State the blood parasite species.
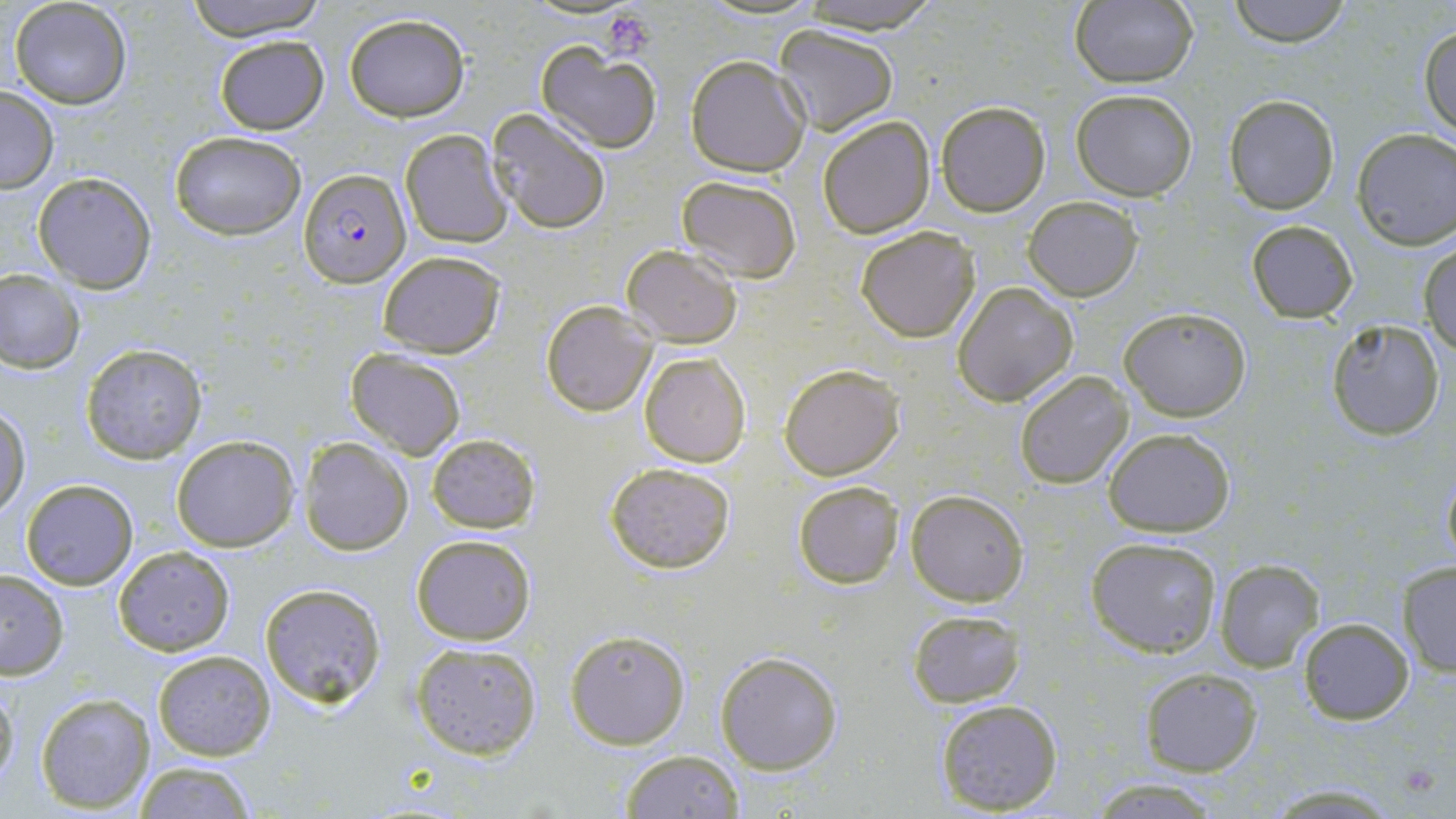

Plasmodium falciparum.

Summary:
  - Coordinate format: approximate bounding boxes as [x1, y1, x2, y2] in pixels
  - Plasmodium falciparum-infected red blood cell locations: [299, 168, 411, 288]
  - Platelet locations: [605, 11, 654, 62]
  - Uninfected red blood cell locations: [10, 0, 132, 108], [180, 0, 331, 42], [790, 0, 945, 33], [1226, 0, 1351, 47], [1068, 1, 1198, 87], [344, 14, 469, 122], [773, 23, 899, 135], [1419, 24, 1456, 140], [214, 35, 328, 133], [535, 42, 662, 154], [685, 57, 810, 177], [0, 86, 60, 193], [1071, 89, 1198, 201], [1224, 94, 1340, 214], [935, 101, 1050, 217], [485, 110, 612, 234], [818, 115, 935, 238], [1351, 129, 1456, 249], [168, 130, 307, 240], [400, 130, 512, 247], [33, 171, 156, 292], [674, 175, 803, 282], [1023, 198, 1142, 302], [1245, 218, 1360, 324], [854, 225, 980, 343], [1420, 241, 1456, 352], [622, 245, 742, 347], [377, 251, 506, 358], [0, 268, 84, 373], [952, 281, 1078, 407], [541, 300, 657, 416], [1120, 307, 1250, 421], [1324, 319, 1448, 441], [81, 344, 207, 464], [346, 349, 466, 458], [640, 350, 752, 469], [778, 362, 905, 480], [1014, 370, 1134, 490], [1, 405, 30, 517], [1103, 427, 1236, 536], [172, 433, 299, 551], [425, 433, 540, 532], [298, 437, 413, 557], [603, 461, 737, 573], [1440, 469, 1456, 570], [20, 479, 138, 590], [792, 479, 906, 588], [905, 490, 1030, 606], [411, 533, 535, 646], [1085, 535, 1223, 657], [111, 545, 236, 656], [1214, 559, 1325, 673], [1397, 561, 1456, 677], [0, 568, 70, 679], [257, 581, 387, 710], [907, 609, 1026, 709], [1297, 617, 1415, 725], [564, 630, 691, 749], [409, 641, 542, 759], [152, 649, 277, 760], [714, 649, 844, 774], [1139, 668, 1263, 777], [0, 676, 18, 790], [35, 690, 156, 813], [936, 699, 1063, 814], [620, 748, 744, 818], [131, 760, 259, 818], [1089, 779, 1223, 816], [1263, 782, 1408, 815]
  - Field of view: one of a larger specimen
  - Image size: 1456×819 pixels
  - Magnification: 1000x
  - Modality: light microscopy
  - Stain: May-Grünwald-Giemsa
  - Preparation: thin blood smear